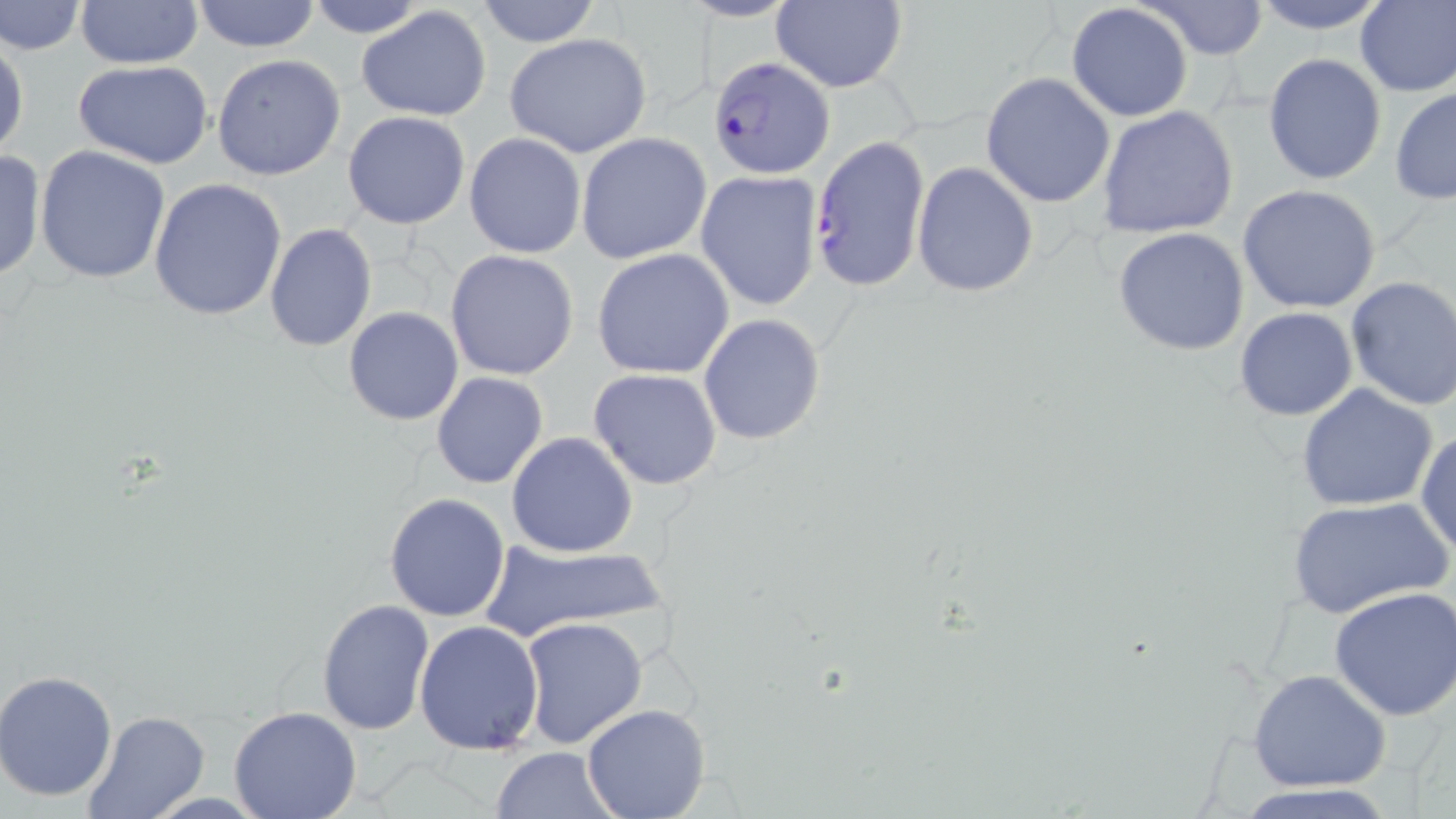
Summary:
  - Coordinate format: approximate bounding boxes as named x1/y1/x2/y2 corners in pixels
  - Plasmodium falciparum-infected red blood cell locations: (x1=708, y1=51, x2=839, y2=176), (x1=808, y1=134, x2=931, y2=293)
  - Uninfected red blood cell locations: (x1=188, y1=0, x2=322, y2=52), (x1=1144, y1=0, x2=1269, y2=59), (x1=1247, y1=0, x2=1394, y2=34), (x1=1355, y1=0, x2=1456, y2=97), (x1=1, y1=1, x2=87, y2=55), (x1=73, y1=1, x2=206, y2=68), (x1=303, y1=1, x2=428, y2=39), (x1=471, y1=1, x2=604, y2=48), (x1=770, y1=2, x2=907, y2=92), (x1=1065, y1=2, x2=1194, y2=122), (x1=357, y1=7, x2=492, y2=122), (x1=504, y1=32, x2=652, y2=158), (x1=1, y1=36, x2=28, y2=161), (x1=1262, y1=52, x2=1387, y2=185), (x1=211, y1=54, x2=346, y2=180), (x1=72, y1=60, x2=216, y2=168), (x1=980, y1=73, x2=1116, y2=209), (x1=1389, y1=87, x2=1456, y2=204), (x1=1097, y1=106, x2=1239, y2=239), (x1=342, y1=111, x2=471, y2=229), (x1=464, y1=132, x2=586, y2=257), (x1=576, y1=132, x2=712, y2=264), (x1=34, y1=145, x2=170, y2=285), (x1=0, y1=148, x2=45, y2=285), (x1=913, y1=161, x2=1039, y2=299), (x1=696, y1=170, x2=823, y2=310), (x1=148, y1=178, x2=288, y2=322), (x1=1238, y1=185, x2=1383, y2=315), (x1=265, y1=224, x2=378, y2=352), (x1=1113, y1=227, x2=1251, y2=357), (x1=592, y1=248, x2=734, y2=379), (x1=445, y1=249, x2=580, y2=381), (x1=1342, y1=275, x2=1456, y2=412), (x1=1234, y1=306, x2=1359, y2=421), (x1=343, y1=307, x2=464, y2=426), (x1=697, y1=314, x2=826, y2=446), (x1=588, y1=368, x2=723, y2=490), (x1=431, y1=371, x2=550, y2=489), (x1=1296, y1=382, x2=1439, y2=512), (x1=1416, y1=430, x2=1456, y2=555), (x1=505, y1=433, x2=638, y2=557), (x1=384, y1=493, x2=511, y2=623), (x1=1284, y1=496, x2=1452, y2=618), (x1=476, y1=537, x2=673, y2=644), (x1=1328, y1=586, x2=1456, y2=720), (x1=316, y1=599, x2=436, y2=737), (x1=519, y1=616, x2=649, y2=749), (x1=414, y1=621, x2=544, y2=754), (x1=1247, y1=669, x2=1391, y2=793), (x1=1, y1=671, x2=119, y2=802), (x1=581, y1=703, x2=711, y2=819), (x1=229, y1=706, x2=363, y2=819), (x1=81, y1=710, x2=209, y2=819), (x1=491, y1=747, x2=621, y2=818), (x1=1226, y1=783, x2=1404, y2=818)
  - Slide-level diagnosis: Plasmodium falciparum
  - Image size: 1456×819 pixels
  - Magnification: 1000x
  - Modality: optical microscopy
  - Field of view: one of a larger specimen
  - Preparation: thin blood film
  - Stain: May-Grünwald-Giemsa